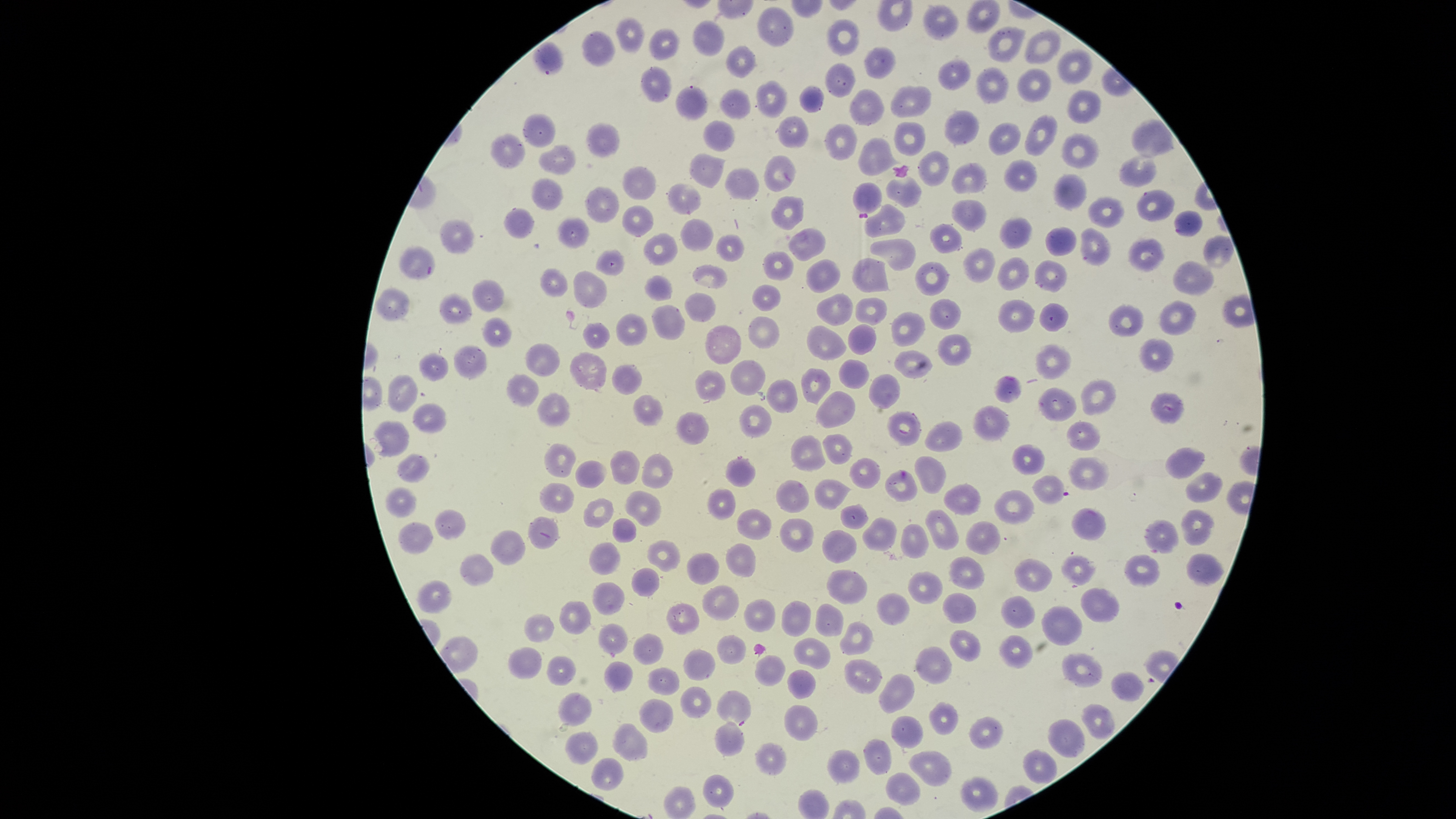
Approximate bounding boxes, in pixels from the top-left corner.
Summary:
  - Uninfected red blood cells: (left=966, top=1, right=1000, bottom=33), (left=922, top=4, right=960, bottom=40), (left=758, top=6, right=794, bottom=48), (left=616, top=17, right=645, bottom=52), (left=826, top=18, right=861, bottom=56), (left=693, top=19, right=725, bottom=55), (left=989, top=26, right=1025, bottom=63), (left=649, top=28, right=679, bottom=60), (left=1025, top=29, right=1061, bottom=64), (left=582, top=31, right=615, bottom=66), (left=725, top=44, right=758, bottom=77), (left=864, top=46, right=896, bottom=79), (left=1057, top=49, right=1091, bottom=85), (left=939, top=58, right=971, bottom=89), (left=825, top=62, right=856, bottom=99), (left=642, top=66, right=672, bottom=103), (left=976, top=67, right=1008, bottom=104), (left=1016, top=67, right=1051, bottom=104), (left=756, top=79, right=786, bottom=117), (left=799, top=84, right=824, bottom=113), (left=891, top=85, right=932, bottom=116), (left=675, top=86, right=709, bottom=122), (left=850, top=88, right=884, bottom=125), (left=720, top=89, right=750, bottom=120), (left=1067, top=90, right=1101, bottom=123), (left=944, top=110, right=980, bottom=145), (left=523, top=113, right=555, bottom=147), (left=1025, top=114, right=1056, bottom=157), (left=777, top=115, right=809, bottom=148), (left=1132, top=119, right=1174, bottom=157), (left=703, top=120, right=734, bottom=152), (left=894, top=120, right=925, bottom=157), (left=586, top=122, right=620, bottom=158), (left=988, top=123, right=1020, bottom=157), (left=825, top=124, right=857, bottom=162), (left=490, top=133, right=525, bottom=169), (left=1062, top=134, right=1099, bottom=169), (left=859, top=136, right=901, bottom=176), (left=539, top=145, right=575, bottom=176), (left=918, top=150, right=949, bottom=186), (left=689, top=153, right=724, bottom=188), (left=1119, top=154, right=1157, bottom=187), (left=764, top=155, right=796, bottom=191), (left=1003, top=159, right=1038, bottom=192), (left=951, top=161, right=988, bottom=194), (left=623, top=166, right=657, bottom=200), (left=724, top=168, right=759, bottom=200), (left=1054, top=174, right=1087, bottom=209), (left=887, top=176, right=923, bottom=207), (left=532, top=179, right=564, bottom=210), (left=852, top=182, right=881, bottom=213), (left=668, top=184, right=701, bottom=214), (left=585, top=187, right=619, bottom=224), (left=1137, top=189, right=1175, bottom=222), (left=772, top=195, right=805, bottom=230), (left=1086, top=197, right=1123, bottom=228), (left=951, top=199, right=986, bottom=231), (left=864, top=204, right=905, bottom=237), (left=622, top=206, right=654, bottom=237), (left=504, top=208, right=535, bottom=240), (left=1174, top=210, right=1202, bottom=237), (left=999, top=216, right=1031, bottom=249), (left=557, top=217, right=589, bottom=249), (left=681, top=217, right=714, bottom=252), (left=439, top=220, right=474, bottom=253), (left=929, top=223, right=961, bottom=253), (left=1046, top=227, right=1076, bottom=257), (left=790, top=228, right=826, bottom=262), (left=1081, top=228, right=1111, bottom=265), (left=643, top=233, right=678, bottom=267), (left=716, top=235, right=745, bottom=262), (left=1202, top=235, right=1233, bottom=269), (left=870, top=238, right=915, bottom=270), (left=1129, top=239, right=1165, bottom=271), (left=399, top=245, right=435, bottom=281), (left=596, top=248, right=625, bottom=276), (left=963, top=249, right=994, bottom=283), (left=762, top=251, right=792, bottom=281), (left=852, top=256, right=889, bottom=293), (left=998, top=257, right=1030, bottom=292), (left=805, top=258, right=841, bottom=292), (left=1034, top=260, right=1067, bottom=292), (left=1173, top=261, right=1215, bottom=295), (left=915, top=262, right=949, bottom=296), (left=693, top=265, right=727, bottom=288), (left=539, top=268, right=568, bottom=297), (left=573, top=271, right=607, bottom=309), (left=645, top=275, right=672, bottom=300), (left=471, top=279, right=504, bottom=314), (left=752, top=285, right=781, bottom=312), (left=377, top=289, right=411, bottom=321), (left=684, top=292, right=717, bottom=323), (left=816, top=292, right=853, bottom=326), (left=440, top=294, right=472, bottom=324), (left=856, top=298, right=888, bottom=326), (left=930, top=298, right=962, bottom=329), (left=1000, top=298, right=1035, bottom=333), (left=1160, top=301, right=1196, bottom=334), (left=1109, top=303, right=1144, bottom=337), (left=651, top=304, right=684, bottom=339), (left=1039, top=304, right=1067, bottom=331), (left=891, top=313, right=926, bottom=346), (left=616, top=314, right=648, bottom=346), (left=482, top=317, right=512, bottom=348), (left=748, top=317, right=780, bottom=348), (left=582, top=321, right=610, bottom=350), (left=704, top=323, right=741, bottom=365), (left=847, top=324, right=876, bottom=356), (left=806, top=325, right=847, bottom=360), (left=938, top=334, right=972, bottom=366), (left=1141, top=338, right=1172, bottom=371), (left=524, top=343, right=560, bottom=376), (left=453, top=344, right=487, bottom=379), (left=1035, top=345, right=1071, bottom=380), (left=895, top=349, right=932, bottom=378), (left=570, top=352, right=607, bottom=389), (left=419, top=353, right=448, bottom=382), (left=730, top=359, right=765, bottom=396), (left=838, top=359, right=869, bottom=389), (left=611, top=364, right=642, bottom=394), (left=801, top=367, right=830, bottom=404), (left=694, top=369, right=726, bottom=402), (left=505, top=373, right=538, bottom=407), (left=387, top=374, right=419, bottom=414), (left=867, top=374, right=900, bottom=409), (left=994, top=375, right=1021, bottom=403), (left=1080, top=378, right=1115, bottom=415), (left=766, top=380, right=798, bottom=414), (left=1038, top=389, right=1076, bottom=422), (left=816, top=390, right=855, bottom=428), (left=537, top=392, right=571, bottom=427), (left=1151, top=393, right=1184, bottom=424), (left=634, top=394, right=663, bottom=427), (left=413, top=403, right=447, bottom=433), (left=973, top=404, right=1011, bottom=441), (left=739, top=405, right=771, bottom=438), (left=887, top=411, right=920, bottom=446), (left=675, top=413, right=709, bottom=446), (left=372, top=420, right=410, bottom=457), (left=925, top=422, right=962, bottom=453), (left=1065, top=422, right=1101, bottom=450), (left=823, top=433, right=851, bottom=463), (left=791, top=435, right=825, bottom=472), (left=543, top=442, right=576, bottom=478), (left=1012, top=444, right=1044, bottom=475), (left=1167, top=447, right=1205, bottom=480), (left=610, top=451, right=639, bottom=485), (left=396, top=453, right=430, bottom=483), (left=642, top=453, right=672, bottom=488), (left=914, top=456, right=946, bottom=493), (left=725, top=457, right=755, bottom=488), (left=1069, top=457, right=1108, bottom=490), (left=849, top=458, right=881, bottom=489), (left=573, top=459, right=606, bottom=488), (left=885, top=470, right=917, bottom=503), (left=1186, top=472, right=1222, bottom=503), (left=1033, top=475, right=1066, bottom=505), (left=814, top=479, right=850, bottom=510), (left=775, top=480, right=809, bottom=513), (left=539, top=482, right=573, bottom=513), (left=944, top=484, right=982, bottom=515), (left=384, top=487, right=416, bottom=518), (left=994, top=488, right=1034, bottom=524), (left=707, top=489, right=736, bottom=519), (left=624, top=490, right=662, bottom=527), (left=584, top=497, right=614, bottom=528), (left=839, top=503, right=868, bottom=528), (left=1072, top=507, right=1106, bottom=541), (left=925, top=508, right=959, bottom=550), (left=736, top=509, right=772, bottom=541), (left=1182, top=509, right=1213, bottom=545), (left=435, top=510, right=466, bottom=540), (left=528, top=517, right=559, bottom=549), (left=611, top=518, right=638, bottom=544), (left=779, top=518, right=814, bottom=552), (left=861, top=518, right=896, bottom=552), (left=1144, top=520, right=1179, bottom=555), (left=398, top=521, right=434, bottom=554), (left=964, top=521, right=1000, bottom=555), (left=901, top=523, right=929, bottom=558), (left=821, top=529, right=858, bottom=563), (left=490, top=530, right=526, bottom=566), (left=648, top=540, right=679, bottom=571), (left=589, top=542, right=620, bottom=576), (left=725, top=543, right=755, bottom=578), (left=687, top=553, right=719, bottom=585), (left=1187, top=553, right=1224, bottom=588), (left=1124, top=554, right=1160, bottom=587), (left=461, top=555, right=493, bottom=587), (left=1063, top=555, right=1095, bottom=586), (left=948, top=557, right=984, bottom=590), (left=1015, top=559, right=1053, bottom=591), (left=631, top=568, right=659, bottom=596), (left=827, top=570, right=868, bottom=605), (left=907, top=571, right=943, bottom=604), (left=417, top=579, right=452, bottom=614), (left=593, top=583, right=624, bottom=615), (left=703, top=585, right=740, bottom=620), (left=1081, top=588, right=1120, bottom=624), (left=877, top=593, right=911, bottom=625), (left=942, top=593, right=977, bottom=624), (left=1001, top=596, right=1036, bottom=630), (left=744, top=598, right=775, bottom=632), (left=558, top=601, right=591, bottom=634), (left=782, top=601, right=811, bottom=636), (left=667, top=602, right=699, bottom=635), (left=816, top=603, right=844, bottom=635), (left=1042, top=606, right=1082, bottom=646), (left=524, top=614, right=553, bottom=643), (left=840, top=621, right=875, bottom=655), (left=599, top=623, right=628, bottom=654), (left=950, top=628, right=981, bottom=662), (left=632, top=632, right=663, bottom=666), (left=717, top=634, right=746, bottom=664), (left=999, top=634, right=1032, bottom=668), (left=793, top=637, right=831, bottom=671), (left=916, top=645, right=953, bottom=685), (left=508, top=646, right=542, bottom=679), (left=682, top=648, right=716, bottom=681), (left=1062, top=652, right=1102, bottom=687), (left=754, top=653, right=786, bottom=688), (left=546, top=654, right=575, bottom=685), (left=845, top=658, right=882, bottom=694), (left=604, top=661, right=634, bottom=693), (left=648, top=667, right=679, bottom=696), (left=787, top=669, right=816, bottom=698), (left=1111, top=670, right=1146, bottom=702), (left=879, top=673, right=914, bottom=713), (left=679, top=685, right=711, bottom=719), (left=558, top=691, right=591, bottom=725), (left=640, top=699, right=673, bottom=733), (left=929, top=701, right=958, bottom=736), (left=1082, top=704, right=1114, bottom=738), (left=783, top=705, right=818, bottom=742), (left=890, top=715, right=924, bottom=749), (left=969, top=717, right=1003, bottom=749), (left=1048, top=719, right=1085, bottom=759), (left=612, top=722, right=648, bottom=762), (left=715, top=722, right=744, bottom=756), (left=567, top=730, right=597, bottom=763), (left=863, top=739, right=892, bottom=775), (left=755, top=744, right=786, bottom=775), (left=828, top=750, right=860, bottom=783), (left=909, top=751, right=951, bottom=786), (left=1023, top=751, right=1057, bottom=783), (left=591, top=757, right=623, bottom=790), (left=885, top=772, right=921, bottom=805), (left=703, top=774, right=733, bottom=807), (left=960, top=776, right=998, bottom=811), (left=663, top=785, right=696, bottom=818)
  - Parasitized red blood cells: (left=532, top=40, right=563, bottom=77), (left=716, top=690, right=751, bottom=727)
  - Preparation: thin blood smear
  - Visible region: circular
  - Presence: malaria parasites identified
  - Field of view: single
  - Capture: smartphone photograph through the microscope eyepiece
  - Species: Plasmodium falciparum
  - Image size: 1456×819 pixels
  - Stain: Giemsa